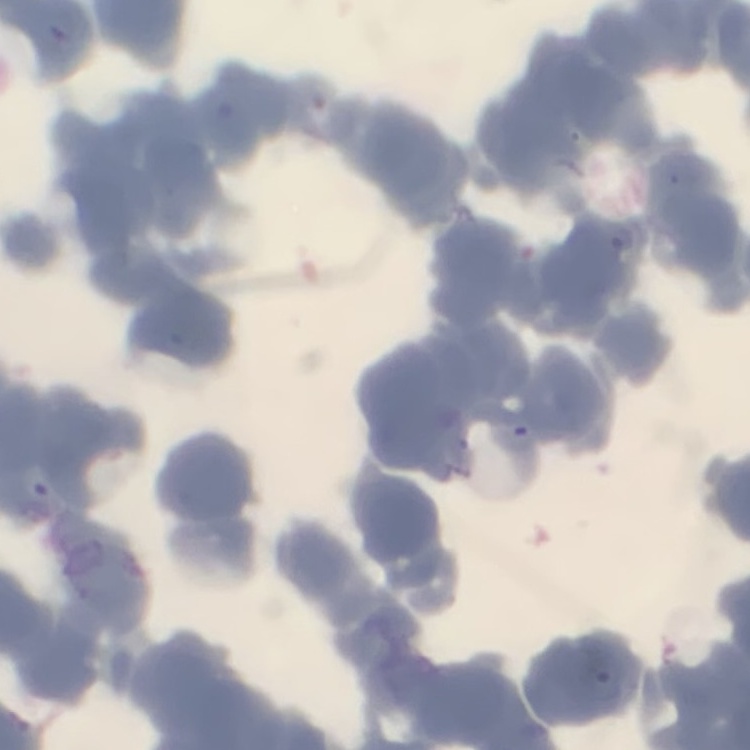

The erythrocytes exhibit rouleaux formation. Thin blood smear. Stained with either Field's or Giemsa. One tile cut from a larger photomicrograph.